Comment on the morphology of the red blood cells.
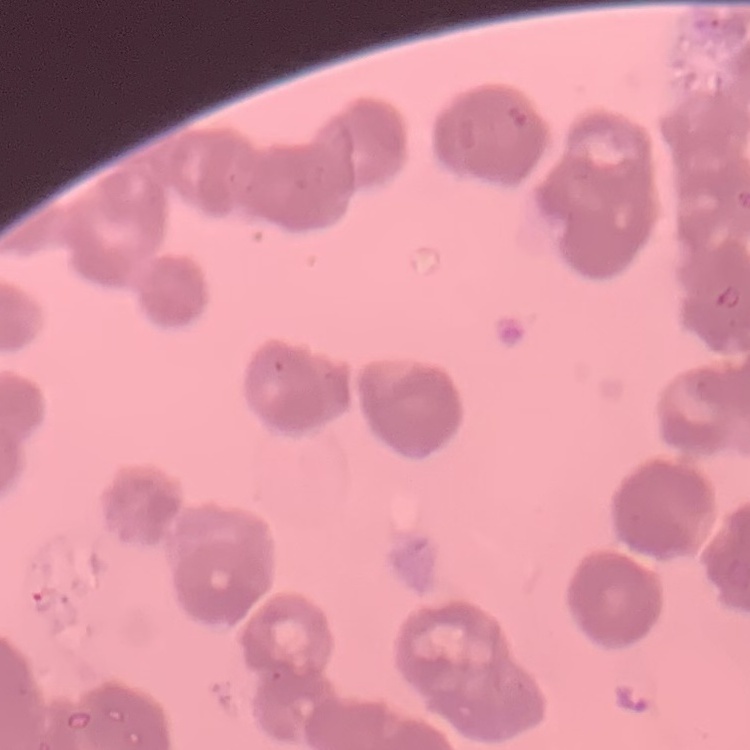

They show rouleaux formation.

Thin blood film. Square crop of a larger photomicrograph. Field's or Giemsa stain.